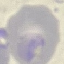

result = no malaria parasites seen
preparation = thin blood smear
stain = Giemsa
image type = automatically extracted cell patch, resized to 64 × 64 pixels
capture = smartphone camera at the microscope eyepiece